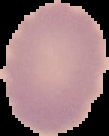
Summary:
  - Image size: 109×136 pixels
  - Result: no malaria parasites detected
  - Image type: segmented cell region with the area outside set to black
  - Preparation: thin blood film